Assess this cell for malaria.
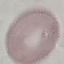
Uninfected.

Summary:
  - Capture: smartphone through the microscope eyepiece
  - Stain: Giemsa
  - Preparation: thin smear
  - Image type: cell patch, automatically extracted from a larger field of view and resized to 64 × 64 pixels